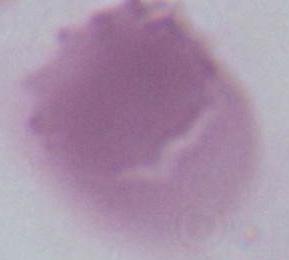

Photomicrograph. Captured at 1000x magnification. A red blood cell is shown.